State which parasite is depicted.
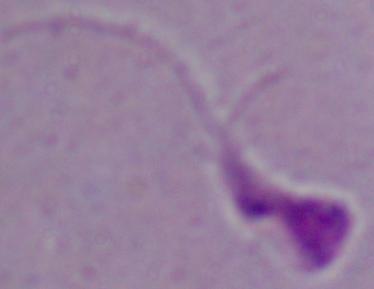
This is Leishmania.

Captured at 1000x magnification. Photomicrograph.